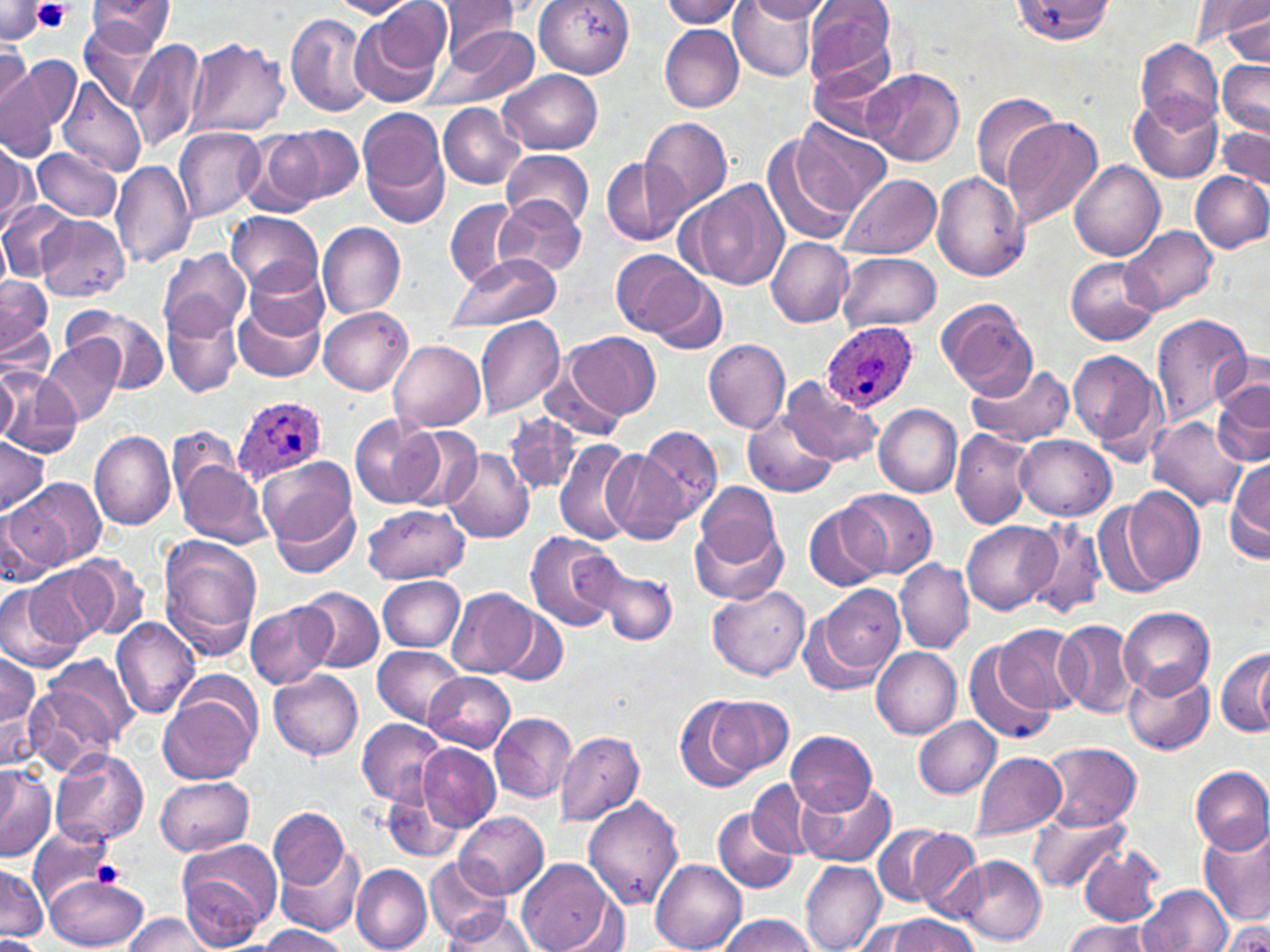
Approximate bounding boxes as (x1, y1, x2, y2) in pixels. Uninfected red blood cell locations: (85, 0, 178, 52), (329, 0, 419, 18), (534, 0, 633, 77), (729, 0, 819, 82), (802, 0, 895, 89), (1189, 0, 1268, 50), (435, 1, 522, 57), (661, 1, 749, 28), (745, 1, 834, 22), (1010, 1, 1115, 44), (0, 3, 50, 44), (353, 3, 450, 104), (1223, 6, 1269, 65), (285, 11, 373, 117), (78, 20, 164, 109), (660, 24, 744, 112), (427, 26, 539, 110), (130, 37, 208, 153), (184, 37, 292, 139), (1135, 39, 1224, 128), (0, 44, 33, 126), (21, 57, 79, 133), (1218, 59, 1270, 137), (811, 66, 898, 148), (1, 67, 55, 162), (864, 68, 964, 167), (498, 69, 603, 154), (58, 79, 148, 180), (971, 90, 1063, 190), (1129, 92, 1222, 184), (439, 104, 526, 189), (358, 110, 451, 229), (643, 117, 734, 214), (1002, 117, 1102, 231), (797, 120, 894, 215), (280, 124, 363, 205), (1216, 125, 1270, 191), (174, 127, 264, 221), (241, 129, 327, 217), (761, 132, 859, 248), (0, 144, 36, 233), (32, 146, 122, 222), (501, 150, 593, 231), (599, 156, 690, 244), (111, 159, 197, 267), (1070, 160, 1164, 261), (1191, 171, 1270, 254), (932, 172, 1029, 281), (838, 174, 940, 260), (685, 178, 791, 292), (497, 197, 588, 277), (444, 198, 525, 290), (0, 201, 77, 281), (227, 211, 323, 295), (36, 215, 130, 301), (317, 222, 405, 319), (1123, 225, 1217, 313), (0, 229, 12, 297), (766, 237, 854, 327), (158, 249, 251, 340), (611, 249, 705, 339), (837, 253, 941, 331), (444, 255, 561, 331), (242, 259, 329, 341), (1065, 259, 1160, 344), (0, 275, 52, 354), (652, 275, 727, 354), (162, 294, 244, 398), (234, 294, 325, 384), (934, 298, 1036, 396), (67, 306, 169, 394), (319, 307, 413, 394), (1150, 313, 1249, 430), (474, 316, 566, 418), (566, 331, 661, 420), (703, 339, 792, 433), (390, 340, 486, 432), (43, 341, 121, 425), (1069, 348, 1165, 461), (1211, 350, 1270, 416), (543, 358, 622, 442), (966, 363, 1076, 447), (0, 364, 20, 442), (2, 369, 82, 457), (779, 376, 883, 468), (1212, 381, 1270, 468), (873, 403, 963, 497), (744, 409, 835, 499), (503, 412, 580, 497), (348, 415, 444, 509), (1149, 416, 1247, 512), (393, 423, 481, 509), (639, 425, 722, 522), (951, 429, 1034, 530), (89, 430, 176, 531), (1015, 434, 1115, 520), (0, 435, 50, 518), (553, 438, 638, 545), (441, 449, 534, 543), (601, 450, 690, 544), (1227, 458, 1270, 561), (177, 460, 271, 548), (261, 463, 359, 575), (9, 477, 102, 570), (696, 483, 779, 563), (1122, 486, 1205, 588), (842, 488, 937, 578), (1094, 497, 1172, 597), (804, 502, 891, 593), (1, 503, 58, 588), (362, 504, 470, 584), (690, 520, 785, 604), (1023, 520, 1105, 622), (962, 521, 1056, 615), (524, 530, 622, 632), (158, 535, 263, 658), (67, 556, 149, 638), (894, 559, 973, 654), (24, 565, 107, 648), (601, 568, 677, 643), (377, 576, 465, 652), (0, 577, 85, 671), (819, 583, 905, 672), (298, 587, 384, 671), (709, 587, 810, 681), (448, 589, 536, 680), (246, 600, 336, 689), (494, 605, 567, 687), (1119, 606, 1214, 697), (800, 611, 890, 696), (110, 616, 199, 719), (1055, 620, 1139, 719), (992, 625, 1087, 716), (964, 638, 1058, 744), (373, 644, 467, 729), (1214, 646, 1269, 739), (871, 648, 961, 738), (1250, 649, 1269, 735), (0, 652, 42, 765), (1123, 665, 1213, 755), (29, 667, 129, 767), (270, 669, 364, 760), (425, 672, 515, 751), (158, 690, 260, 784), (675, 695, 765, 792), (711, 697, 795, 776), (491, 713, 576, 802), (914, 717, 1000, 799), (358, 719, 447, 805), (787, 729, 876, 814), (555, 730, 644, 827), (420, 743, 500, 830), (1038, 743, 1141, 828), (51, 748, 149, 846), (969, 751, 1065, 841), (0, 763, 55, 863), (1191, 766, 1270, 854), (383, 768, 468, 864), (156, 775, 253, 856), (748, 779, 815, 858), (797, 780, 896, 867), (583, 797, 684, 909), (268, 806, 352, 891), (712, 807, 797, 894), (1027, 809, 1130, 893), (455, 811, 549, 899), (28, 824, 118, 906), (867, 824, 972, 909), (1200, 824, 1270, 926), (275, 840, 365, 937), (176, 841, 279, 949), (1079, 843, 1167, 926), (949, 855, 1047, 945), (425, 856, 508, 942), (518, 857, 613, 952), (651, 861, 747, 952), (1, 862, 47, 940), (800, 862, 886, 952), (352, 864, 432, 952), (44, 874, 146, 950), (1138, 886, 1233, 952), (440, 906, 538, 950), (124, 913, 219, 951), (721, 914, 818, 952), (885, 915, 978, 952), (1223, 916, 1270, 952), (857, 919, 931, 952), (1061, 920, 1153, 952), (256, 926, 347, 952), (0, 935, 42, 952). Plasmodium ovale-infected red blood cell locations: (822, 322, 916, 414), (233, 394, 326, 485). Platelet locations: (33, 0, 72, 34), (91, 860, 124, 889). Slide-level diagnosis: Plasmodium ovale. Image is 1270×952 pixels. Thin blood film. Light microscopy. May-Grünwald-Giemsa-stained preparation. Captured at 1000x magnification. One field of a larger specimen.